Give the extent of all uninfected red blood cells.
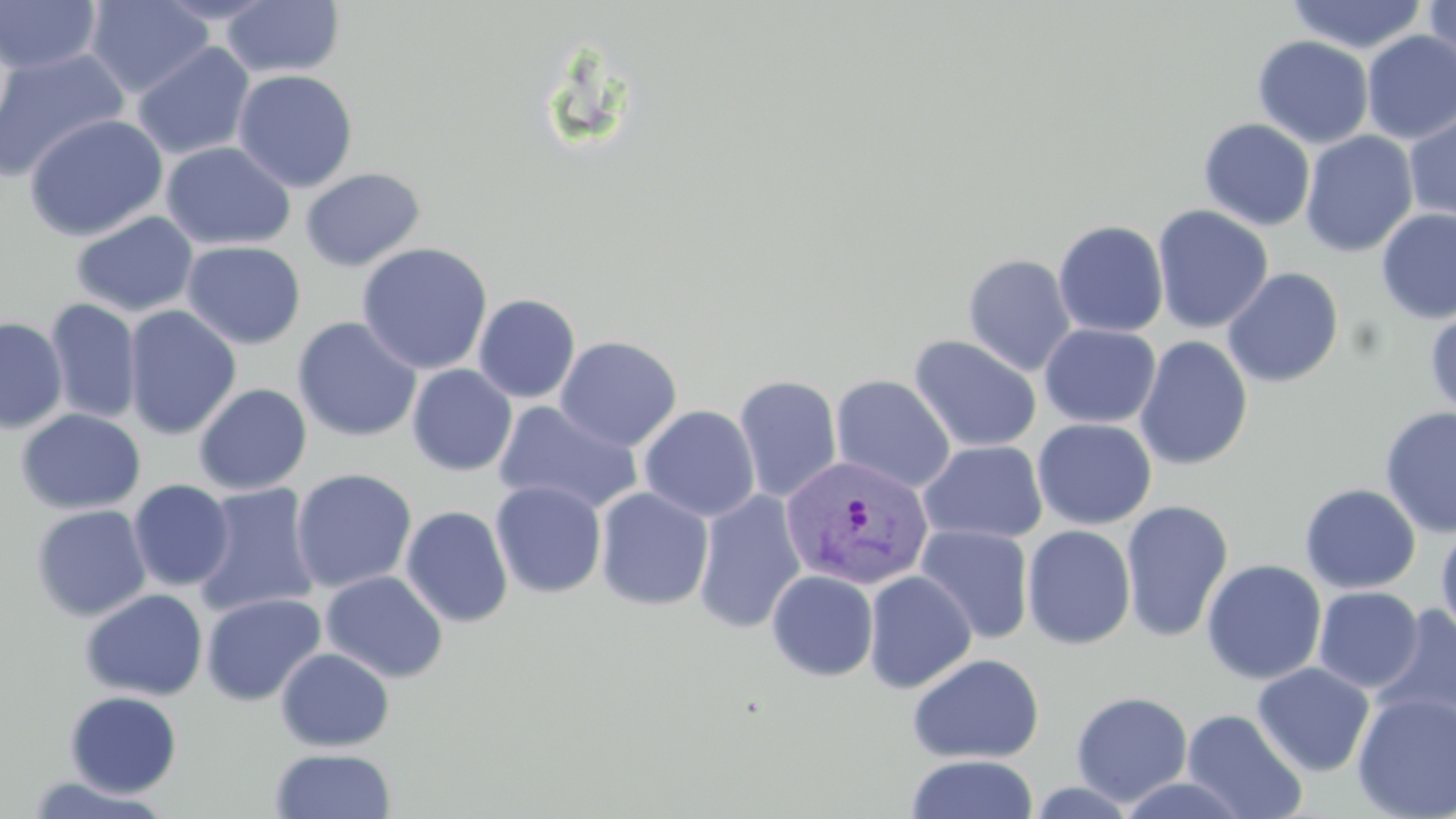

Approximate bounding boxes as (x1, y1, x2, y2) in pixels.
Uninfected red blood cells: (0, 0, 102, 75), (85, 0, 214, 98), (151, 0, 280, 24), (220, 0, 346, 79), (1287, 0, 1428, 54), (1422, 0, 1455, 78), (1361, 30, 1456, 144), (1252, 35, 1374, 149), (132, 41, 255, 160), (0, 49, 131, 183), (232, 69, 359, 192), (1403, 110, 1456, 224), (24, 113, 168, 242), (1198, 118, 1315, 231), (1300, 130, 1419, 257), (160, 141, 296, 252), (301, 167, 426, 272), (1152, 205, 1274, 333), (1376, 209, 1456, 324), (70, 211, 198, 317), (1053, 220, 1169, 338), (182, 241, 305, 349), (357, 242, 493, 375), (962, 253, 1077, 376), (1222, 267, 1344, 388), (473, 294, 581, 403), (45, 298, 142, 424), (1425, 304, 1456, 420), (123, 305, 242, 439), (292, 316, 422, 443), (0, 317, 67, 434), (1039, 323, 1161, 427), (908, 334, 1042, 453), (554, 335, 683, 451), (1135, 336, 1254, 471), (406, 364, 518, 477), (733, 374, 843, 502), (830, 374, 956, 493), (193, 383, 312, 495), (494, 401, 644, 517), (639, 405, 760, 522), (1379, 406, 1456, 539), (16, 408, 145, 515), (1033, 418, 1157, 529), (918, 440, 1047, 545), (291, 468, 417, 594), (128, 479, 235, 591), (490, 480, 607, 598), (192, 483, 319, 617), (1300, 483, 1421, 594), (595, 487, 714, 611), (693, 489, 807, 634), (1120, 499, 1234, 643), (30, 504, 152, 622), (400, 505, 514, 628), (1436, 522, 1456, 645), (915, 524, 1035, 644), (1022, 524, 1137, 650), (1201, 559, 1327, 685), (766, 569, 879, 681), (321, 570, 448, 683), (863, 570, 977, 693), (1312, 586, 1424, 693), (80, 588, 208, 701), (200, 592, 326, 706), (1371, 602, 1456, 739), (275, 647, 395, 752), (907, 652, 1045, 764), (1252, 662, 1375, 777), (64, 690, 182, 797), (1071, 691, 1193, 807), (1352, 691, 1456, 818), (1181, 708, 1307, 819), (270, 748, 396, 819), (906, 754, 1039, 819), (22, 774, 172, 818), (1114, 774, 1253, 818), (1027, 780, 1140, 818).

Plasmodium vivax-infected red blood cell locations: (780, 454, 934, 591). Slide-level diagnosis: Plasmodium vivax. May-Grünwald-Giemsa stain. Image is 1456×819 pixels. Optical microscopy. Thin blood film. Captured at 1000x magnification. Single field of view.